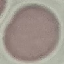
Malaria status: uninfected. Giemsa-stained preparation. Automatically extracted cell patch, resized to 64 × 64 pixels. Photographed with a smartphone camera at the microscope eyepiece. Thin blood film.